Name the parasite shown.
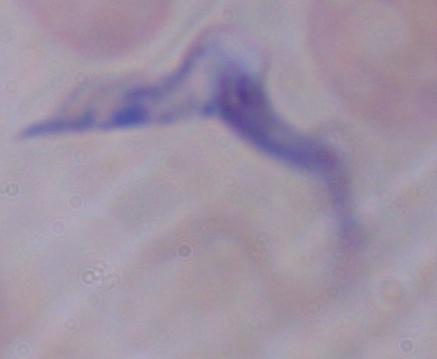

This is a trypanosome.

1000x magnification. Micrograph.